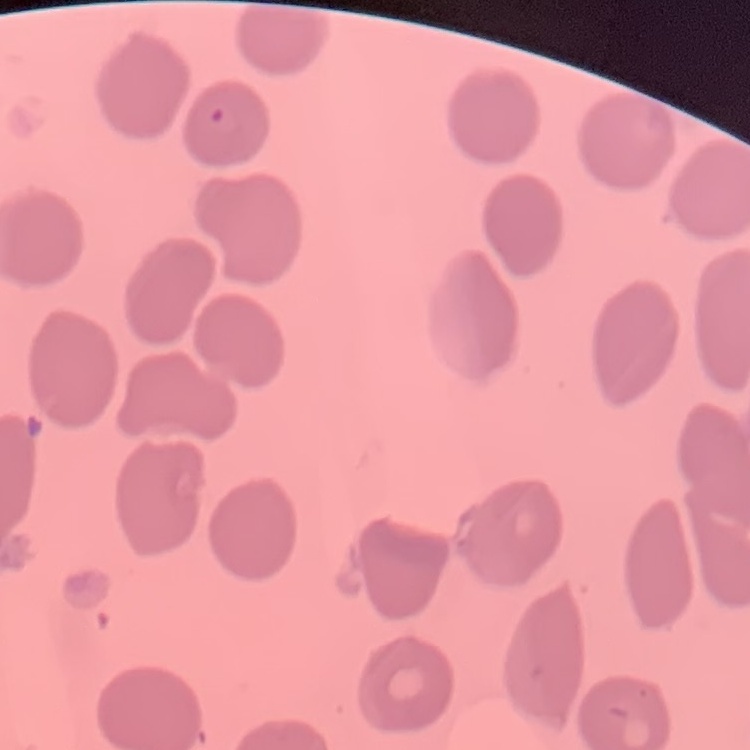

The red blood cells show no rouleaux formation. Stained with either Field's or Giemsa. Square crop of a larger photomicrograph. Thin peripheral smear.